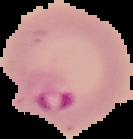

image size = 133×139 pixels
image type = segmented cell region with the area outside set to black
preparation = thin blood smear
malaria status = parasitized